Assess this cell for malaria.
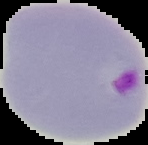
It is parasitized.

Image is 148×145 pixels. Cell region segmented out of the field of view; the surrounding area is masked to black. From a thin blood film.